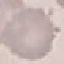
result = no malaria parasites seen
image type = automatically extracted cell patch, resized to 64 × 64 pixels
stain = Giemsa
preparation = thin blood film
capture = smartphone camera at the microscope eyepiece